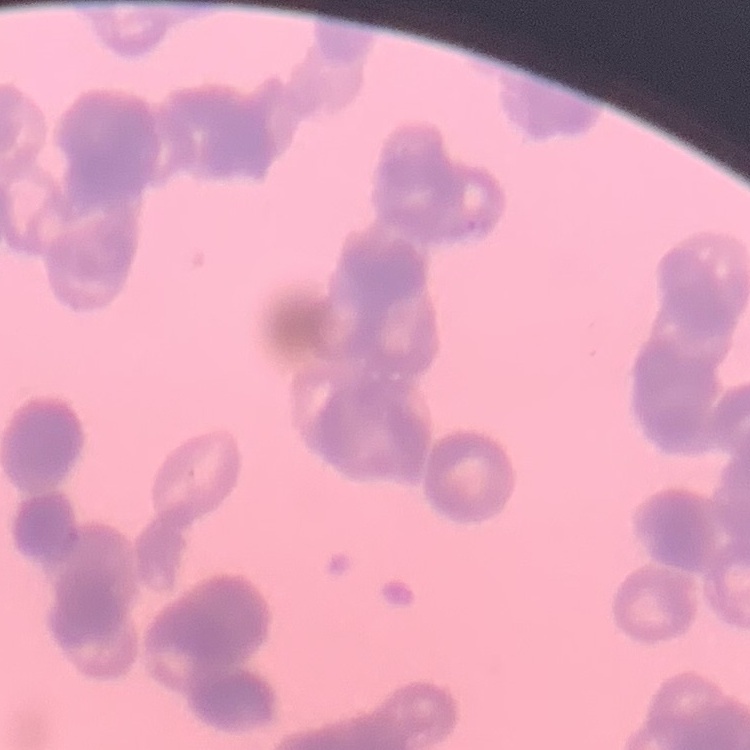

erythrocyte morphology = rouleaux formation
stain = Field's or Giemsa
preparation = thin blood smear
image type = square crop of a larger photomicrograph